Locate every Plasmodium parasite.
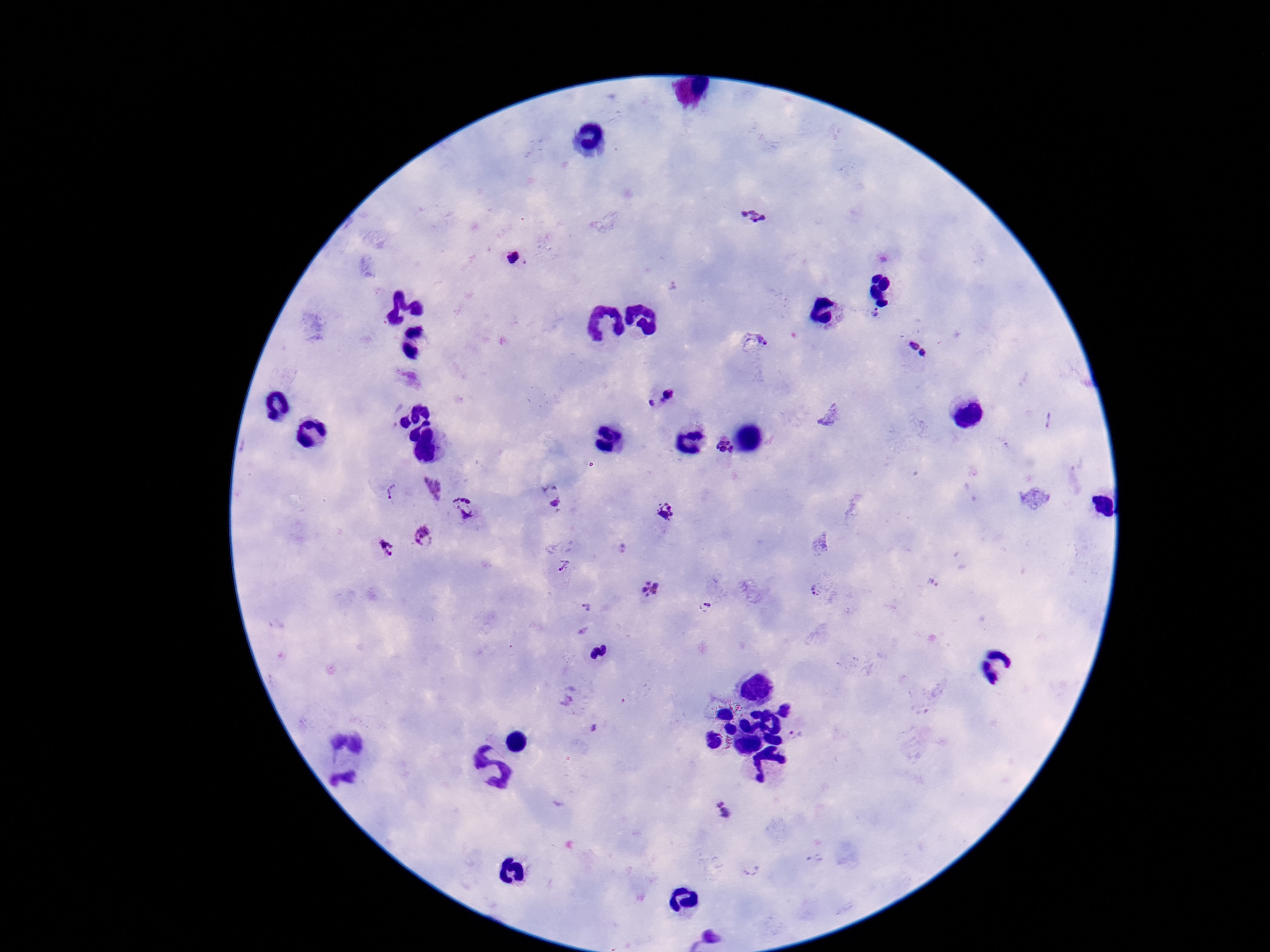

Approximate centers as (x, y) in pixels.
Plasmodium parasites: (751, 216), (514, 257), (877, 314), (753, 346), (919, 351), (659, 398), (724, 450), (429, 488), (391, 492), (558, 505), (463, 507), (665, 515), (425, 537), (386, 546), (563, 565), (650, 590), (817, 590), (707, 607), (584, 609), (796, 734), (724, 809).

patient malaria status = infected
magnification = 100x
preparation = thick peripheral-blood smear
stain = Giemsa
image size = 1270×952 pixels
field of view = single
capture = smartphone camera through the microscope eyepiece